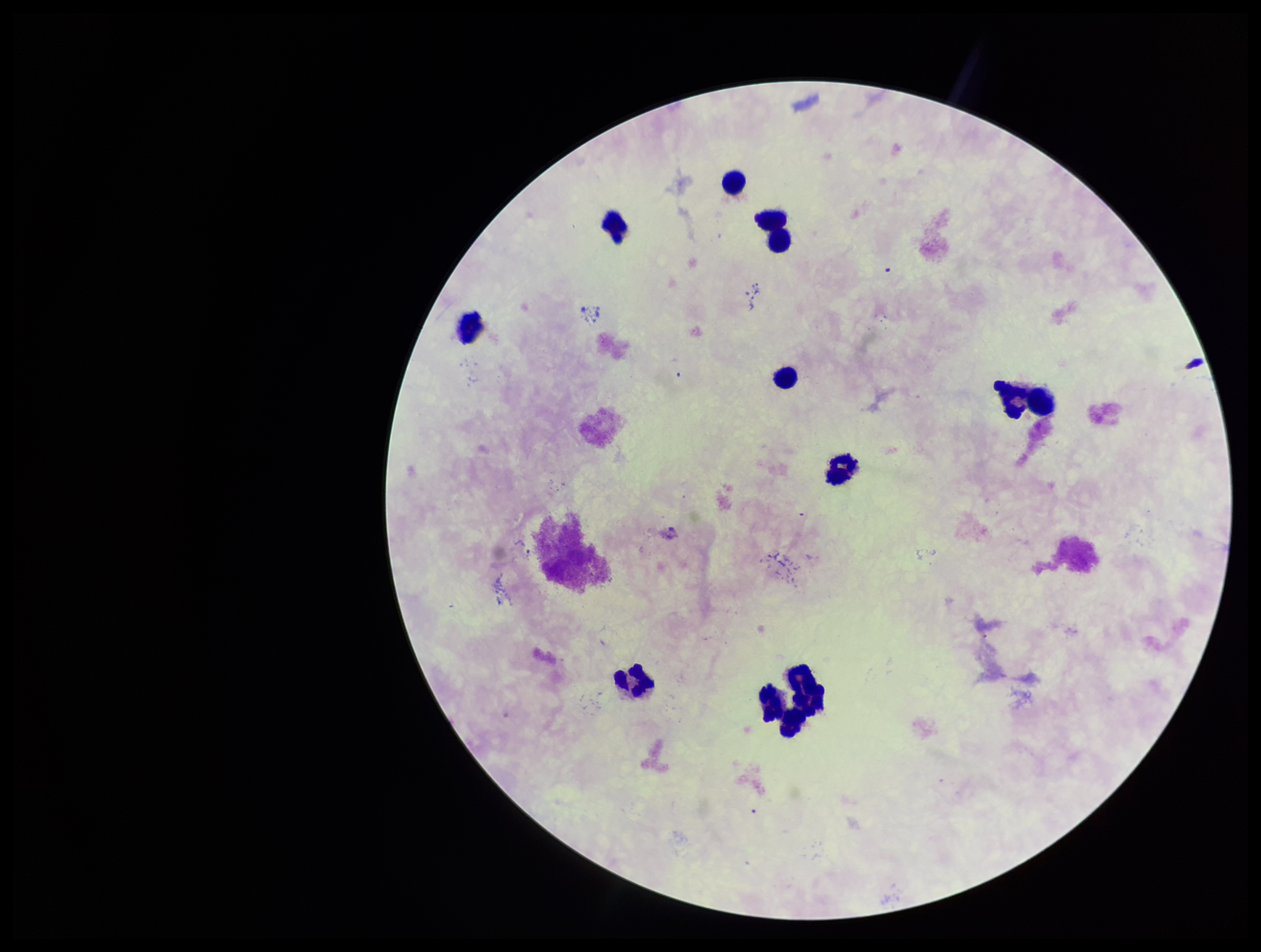

Summary:
  - Plasmodium parasites: none detected
  - Capture: smartphone photograph through the microscope eyepiece
  - Patient malaria status: negative
  - Stain: Giemsa
  - Field of view: single
  - Preparation: thick smear
  - Parasite count: 0
  - Image size: 1261×952 pixels
  - Leukocyte count: 11